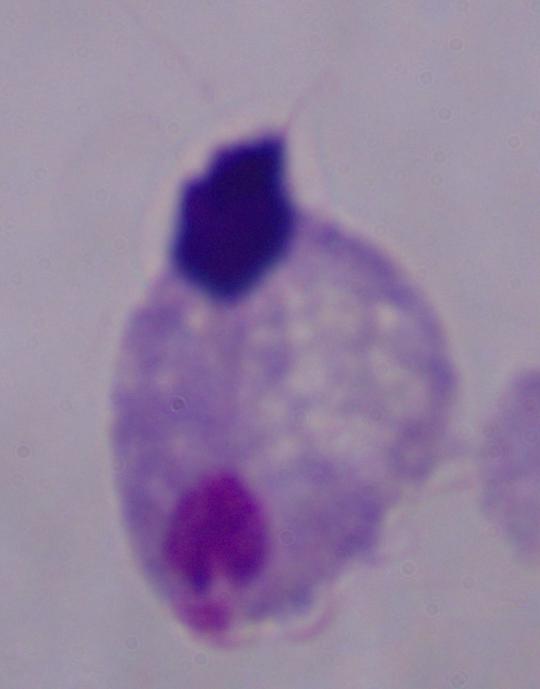 1000x magnification. Photomicrograph. A trichomonad is shown.